Report the malaria status of this cell.
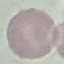

Uninfected.

Acquired by smartphone through the microscope eyepiece. Cell patch, automatically extracted from a larger field of view and resized to 64 × 64 pixels. Thin smear of blood. Giemsa stain.